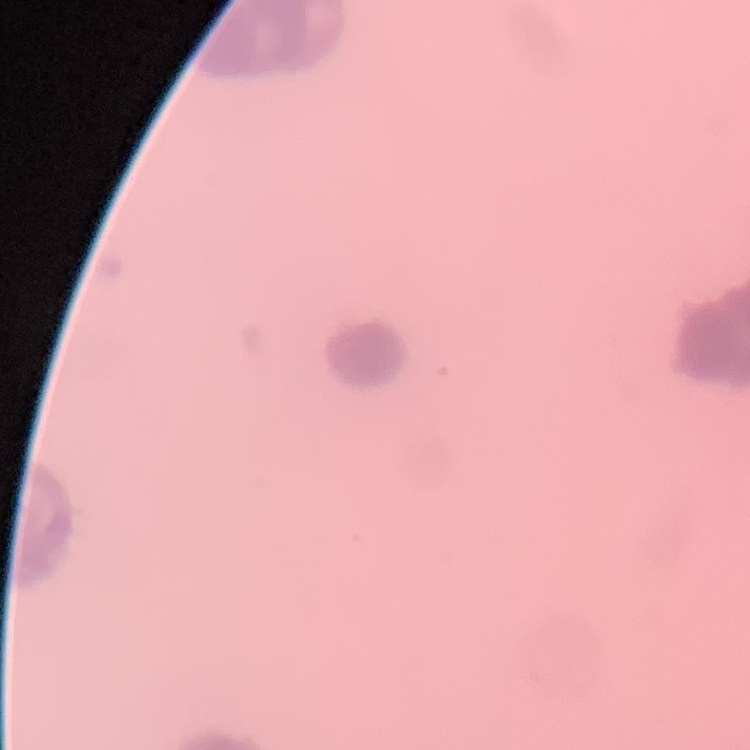

Summary:
  - Erythrocyte morphology: rouleaux formation
  - Preparation: thin blood smear
  - Stain: Field's or Giemsa
  - Image type: square crop of a larger photomicrograph